Outline each uninfected red blood cell.
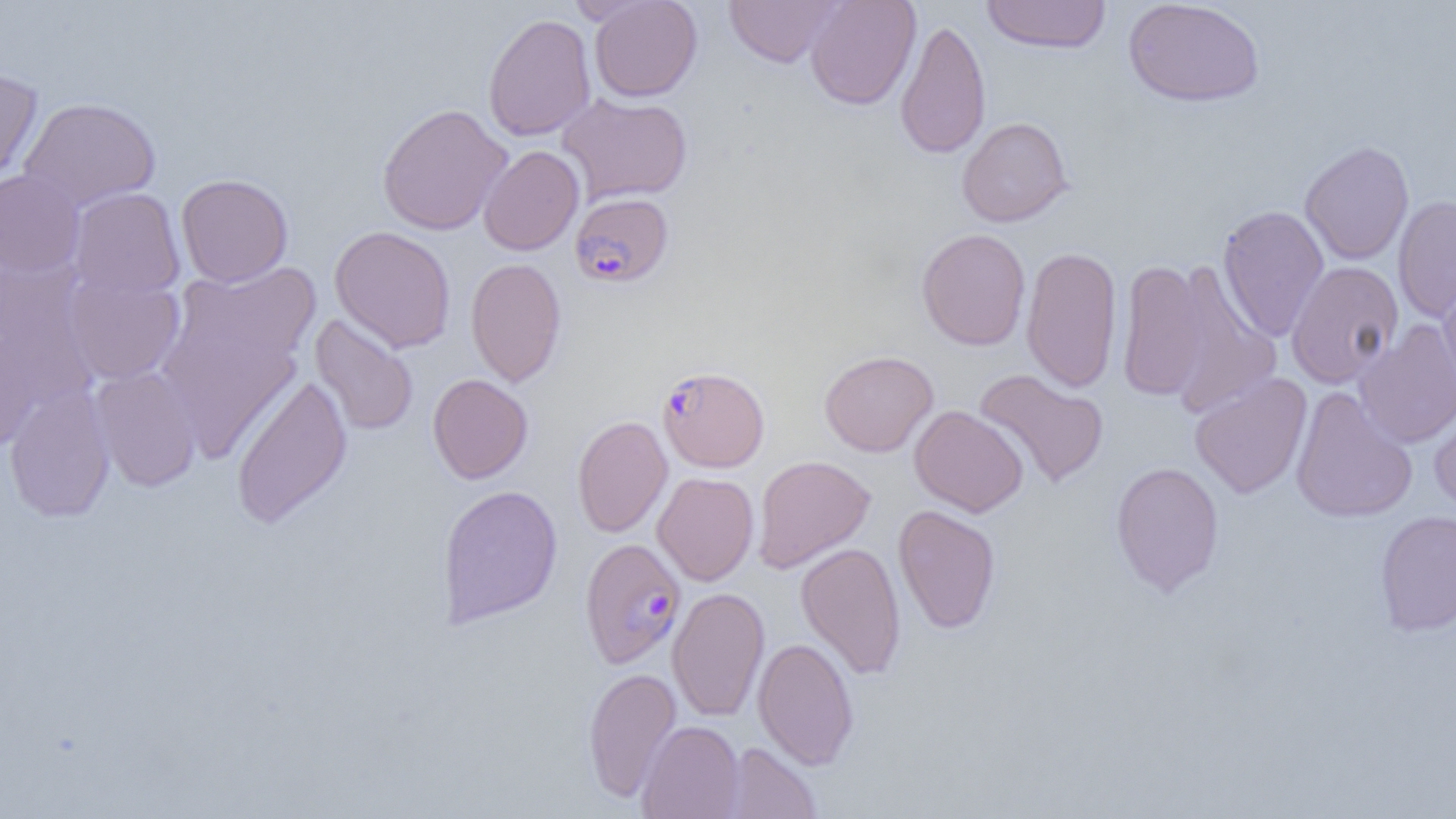

Approximate bounding boxes as (x1, y1, x2, y2) in pixels.
Uninfected red blood cells: (566, 0, 661, 27), (588, 0, 702, 102), (724, 0, 845, 68), (804, 0, 921, 111), (980, 0, 1111, 54), (1123, 1, 1265, 107), (483, 13, 596, 141), (895, 18, 991, 160), (0, 67, 44, 191), (557, 92, 693, 205), (19, 97, 161, 212), (377, 103, 512, 236), (957, 117, 1073, 228), (1300, 140, 1414, 265), (478, 145, 584, 256), (0, 169, 84, 278), (175, 173, 293, 287), (68, 187, 186, 300), (1393, 195, 1456, 323), (1217, 205, 1330, 342), (329, 225, 456, 353), (916, 228, 1031, 351), (1021, 244, 1123, 393), (465, 257, 567, 388), (1117, 259, 1208, 403), (1166, 259, 1281, 418), (1286, 260, 1404, 388), (171, 261, 322, 370), (0, 262, 99, 409), (64, 272, 186, 385), (1438, 278, 1456, 401), (310, 313, 419, 436), (158, 320, 303, 462), (1354, 320, 1456, 449), (0, 328, 44, 450), (819, 350, 938, 457), (90, 366, 203, 492), (973, 368, 1109, 489), (230, 373, 353, 529), (427, 373, 533, 484), (1189, 373, 1312, 499), (4, 384, 116, 522), (1290, 387, 1417, 523), (1428, 397, 1456, 518), (909, 405, 1029, 517), (572, 415, 672, 538), (752, 455, 875, 573), (1110, 461, 1225, 597), (652, 472, 759, 586), (437, 484, 563, 628), (893, 504, 1001, 635), (1375, 510, 1456, 637), (795, 542, 907, 681), (667, 587, 770, 722), (753, 637, 859, 770), (582, 666, 682, 803), (637, 720, 744, 819), (722, 741, 823, 819).

Summary:
  - Plasmodium falciparum-infected red blood cell locations: (570, 192, 674, 288), (658, 366, 770, 472), (579, 537, 686, 669)
  - Slide-level diagnosis: Plasmodium falciparum
  - Magnification: 1000x
  - Modality: light microscopy
  - Preparation: thin blood film
  - Field of view: single
  - Image size: 1456×819 pixels